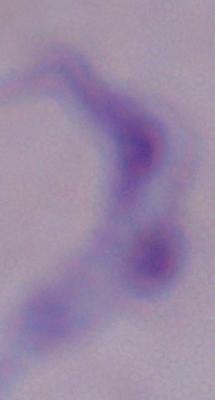

Micrograph. A trypanosome is shown. 1000x magnification.